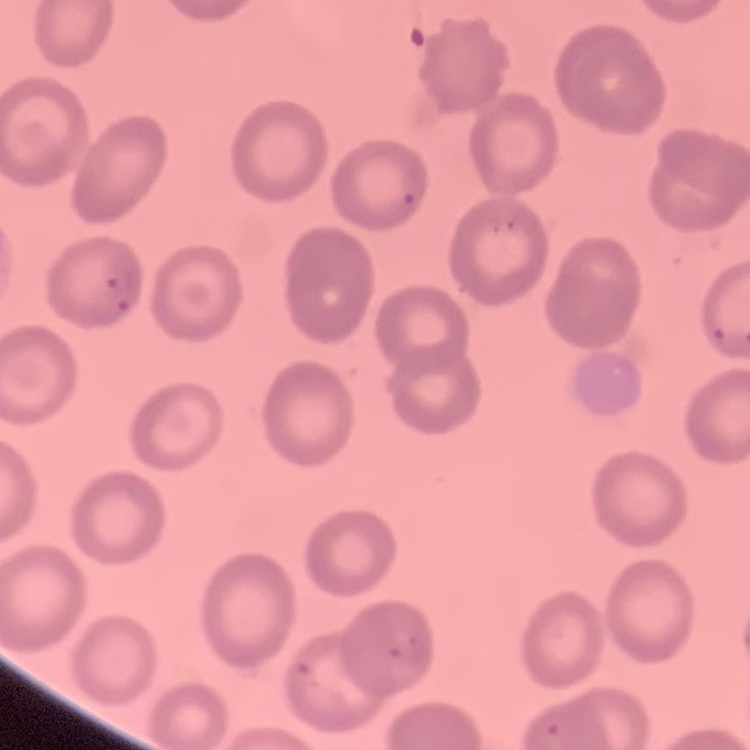
erythrocyte_morphology: no rouleaux formation
image_type: one tile cut from a larger photomicrograph
preparation: thin peripheral smear
stain: Field's or Giemsa